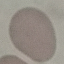

malaria status = uninfected
preparation = thin blood film
image type = cell patch, automatically extracted from a larger field of view and resized to 64 × 64 pixels
capture = smartphone through the microscope eyepiece
stain = Giemsa